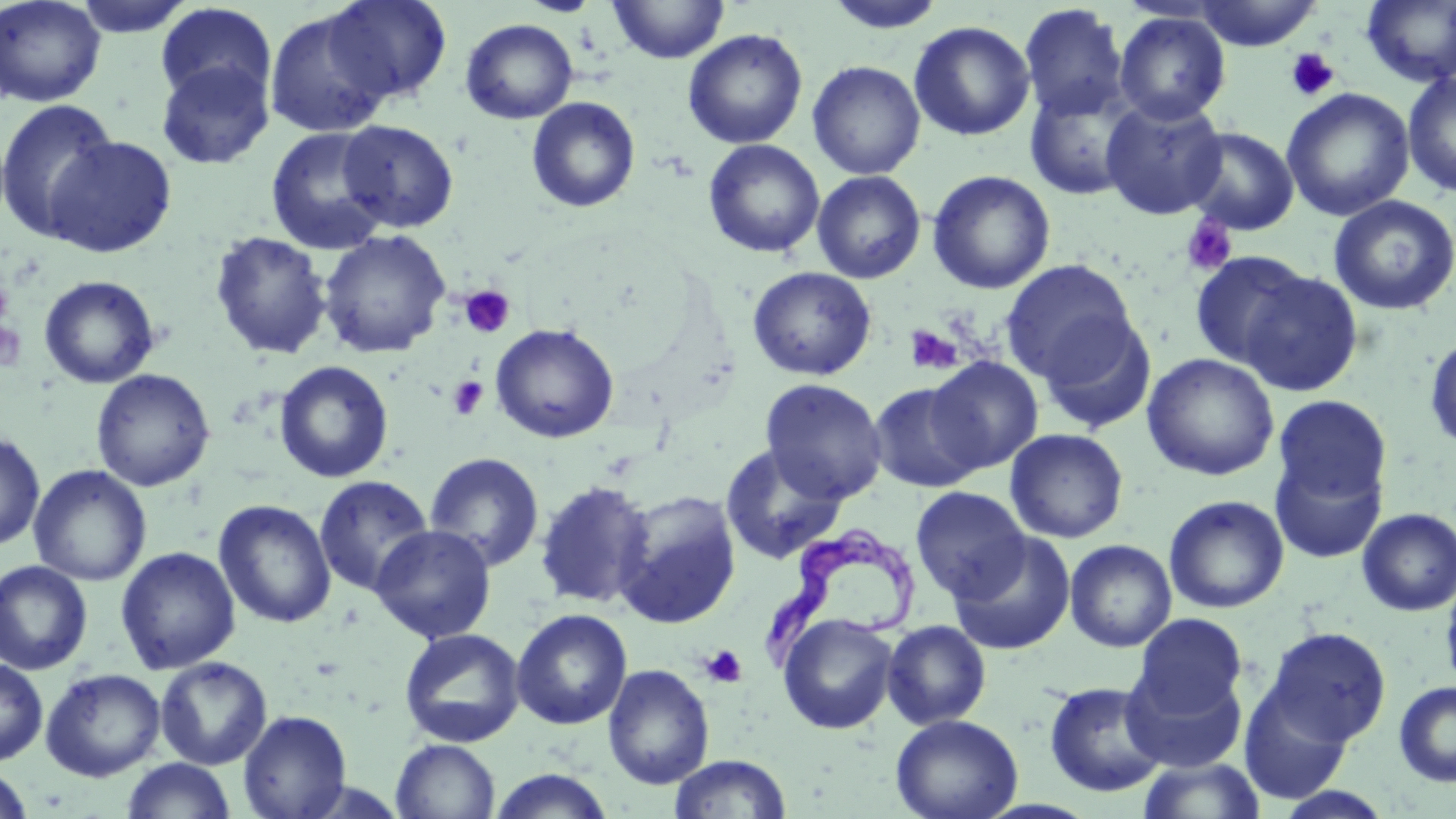
Summary:
  - Coordinate format: approximate bounding boxes as (x1,y1)-(x2,y2) corner pairs in pixels
  - Trypanosoma brucei locations: (762,522)-(920,676)
  - Uninfected red blood cell locations: (0,0)-(107,107), (71,0)-(198,38), (322,0)-(453,104), (520,0)-(603,17), (609,0)-(729,64), (823,0)-(949,35), (1191,0)-(1323,50), (1361,1)-(1456,88), (155,3)-(277,107), (1018,4)-(1130,122), (263,10)-(394,138), (1114,11)-(1231,125), (460,18)-(579,124), (909,21)-(1035,141), (683,28)-(807,149), (155,60)-(274,169), (807,60)-(926,179), (1402,70)-(1456,198), (1023,78)-(1145,200), (1280,88)-(1415,222), (526,97)-(641,213), (1100,97)-(1229,219), (0,98)-(121,243), (337,119)-(458,233), (1181,126)-(1300,235), (266,127)-(392,254), (42,135)-(177,258), (703,139)-(825,259), (812,170)-(926,284), (927,170)-(1056,295), (1328,195)-(1456,315), (317,230)-(452,358), (209,231)-(333,360), (1189,251)-(1312,370), (999,260)-(1137,382), (747,266)-(877,381), (1239,270)-(1363,398), (38,275)-(160,389), (1037,311)-(1156,435), (490,322)-(620,443), (1424,332)-(1456,455), (1142,353)-(1279,481), (927,356)-(1043,473), (273,360)-(394,483), (90,368)-(216,492), (759,378)-(887,503), (868,382)-(986,493), (1273,395)-(1392,507), (1005,428)-(1129,543), (0,430)-(45,552), (719,443)-(847,565), (1271,451)-(1387,563), (423,452)-(544,572), (28,465)-(151,587), (313,475)-(434,597), (534,480)-(657,610), (910,486)-(1030,602), (613,491)-(742,629), (1164,495)-(1289,613), (214,499)-(337,629), (1357,508)-(1456,617), (370,524)-(497,643), (948,530)-(1076,655), (1064,539)-(1177,652), (115,546)-(241,674), (0,560)-(93,675), (1440,576)-(1456,693), (511,608)-(633,730), (777,613)-(899,734), (1133,614)-(1248,718), (882,619)-(991,729), (398,627)-(526,748), (1264,627)-(1391,746), (155,656)-(272,770), (0,657)-(48,765), (603,664)-(715,789), (1123,666)-(1246,773), (40,668)-(166,782), (1044,681)-(1168,798), (1394,681)-(1456,787), (1238,684)-(1353,804), (237,709)-(352,819), (890,713)-(1023,819), (390,739)-(500,819), (668,753)-(792,818), (1138,756)-(1267,819), (121,757)-(236,818), (1,766)-(35,818), (486,768)-(617,818)
  - Platelet locations: (1284,48)-(1340,101), (1181,216)-(1237,276), (0,278)-(13,324), (460,285)-(515,338), (0,319)-(26,372), (904,325)-(964,375), (447,376)-(489,420), (699,645)-(747,688)
  - Slide-level diagnosis: Trypanosoma brucei
  - Preparation: thin blood film
  - Stain: May-Grünwald-Giemsa
  - Modality: optical microscopy
  - Image size: 1456×819 pixels
  - Magnification: 1000x
  - Field of view: single